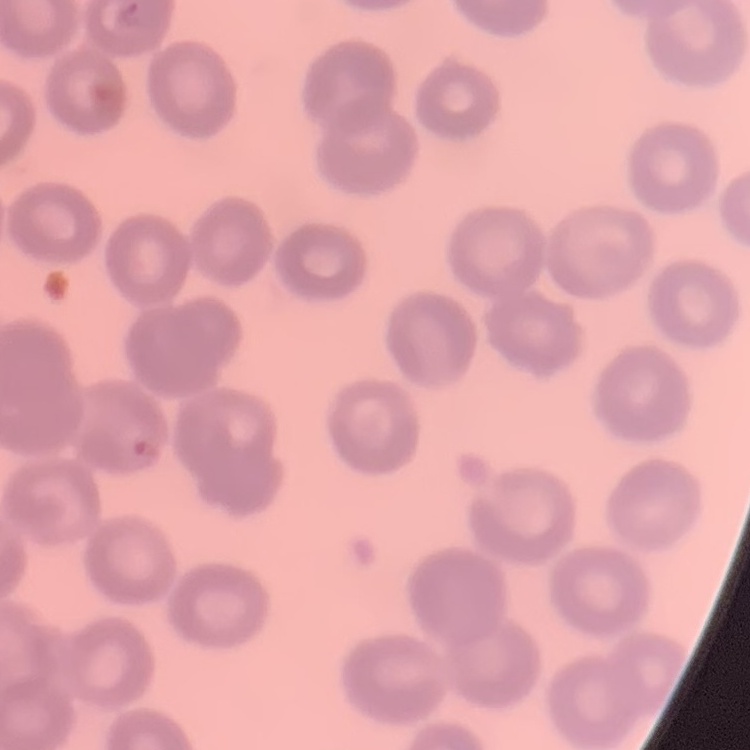
The erythrocytes exhibit no rouleaux formation. Thin peripheral smear. Stained with either Field's or Giemsa. Square crop of a larger photomicrograph.